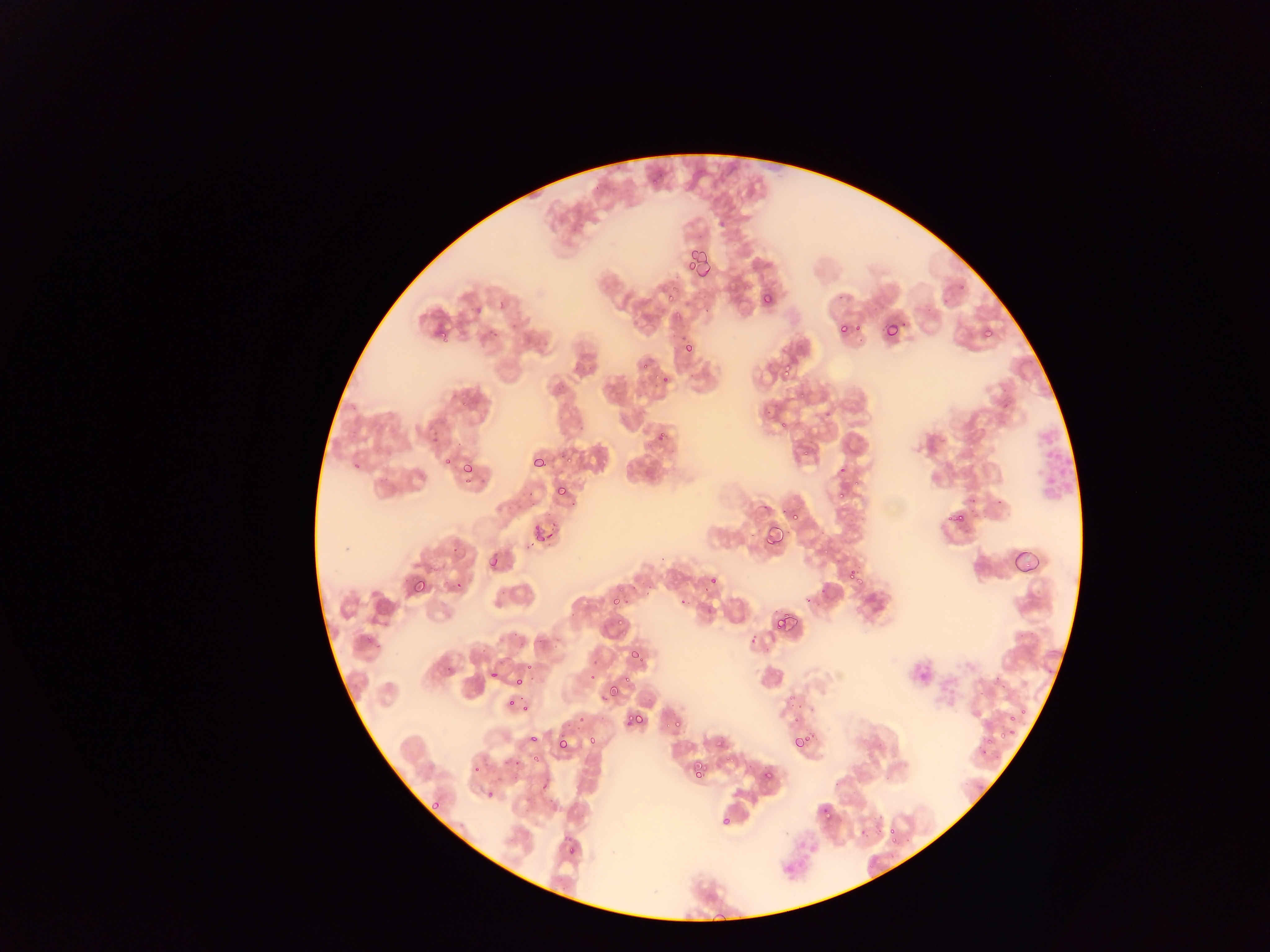

{
  "capture": "mobile-phone photograph through a microscope",
  "leukocyte_locations": "approximate bounding boxes as (left, top, right, bottom) in pixels: (1033, 415, 1077, 507)",
  "preparation": "thin blood smear",
  "field_of_view": "single",
  "image_size": "1270×952 pixels",
  "plasmodium_parasite_locations": "approximate bounding boxes as (left, top, right, bottom) in pixels: (649, 176, 657, 185), (696, 254, 709, 278), (685, 260, 697, 270), (662, 289, 682, 306), (761, 293, 773, 305), (838, 321, 851, 336), (883, 322, 901, 340), (854, 323, 862, 331), (436, 328, 448, 340), (983, 328, 994, 338), (684, 343, 694, 353), (638, 360, 649, 370), (780, 360, 794, 375), (660, 375, 669, 385), (799, 390, 808, 401), (779, 421, 789, 429), (653, 423, 668, 447), (802, 443, 815, 459), (565, 452, 573, 463), (533, 456, 547, 467), (442, 457, 453, 468), (352, 462, 360, 469), (463, 463, 474, 474), (854, 481, 860, 489), (838, 483, 853, 497), (556, 486, 567, 497), (952, 509, 965, 523), (788, 510, 800, 521), (530, 517, 559, 546), (761, 523, 785, 547), (451, 545, 460, 554), (1010, 546, 1040, 572), (489, 555, 500, 568), (847, 568, 862, 586), (410, 576, 427, 594), (709, 576, 718, 584), (453, 581, 462, 591), (618, 583, 625, 593), (609, 597, 619, 607), (775, 612, 794, 631), (616, 619, 624, 628), (629, 649, 640, 660), (523, 659, 535, 668), (592, 659, 603, 666), (490, 669, 499, 680), (589, 670, 598, 686), (514, 677, 524, 687), (622, 677, 632, 683), (609, 688, 621, 701), (785, 695, 801, 709), (507, 697, 517, 707), (522, 703, 530, 712), (1019, 709, 1028, 719), (623, 711, 634, 726), (633, 713, 645, 724), (1009, 714, 1017, 722), (578, 715, 587, 724), (791, 716, 803, 724), (672, 719, 683, 731), (999, 732, 1010, 742), (528, 735, 540, 745), (792, 735, 804, 747), (555, 737, 569, 750), (587, 737, 597, 746), (715, 737, 727, 748), (804, 737, 812, 742), (984, 738, 994, 748), (510, 757, 521, 768), (692, 762, 705, 776), (472, 764, 481, 775), (762, 770, 772, 780), (485, 792, 494, 800), (431, 803, 440, 809), (819, 805, 833, 818), (720, 814, 732, 826), (887, 825, 897, 835), (890, 836, 902, 844), (567, 846, 576, 855), (705, 891, 718, 904)",
  "country": "Ghana"
}